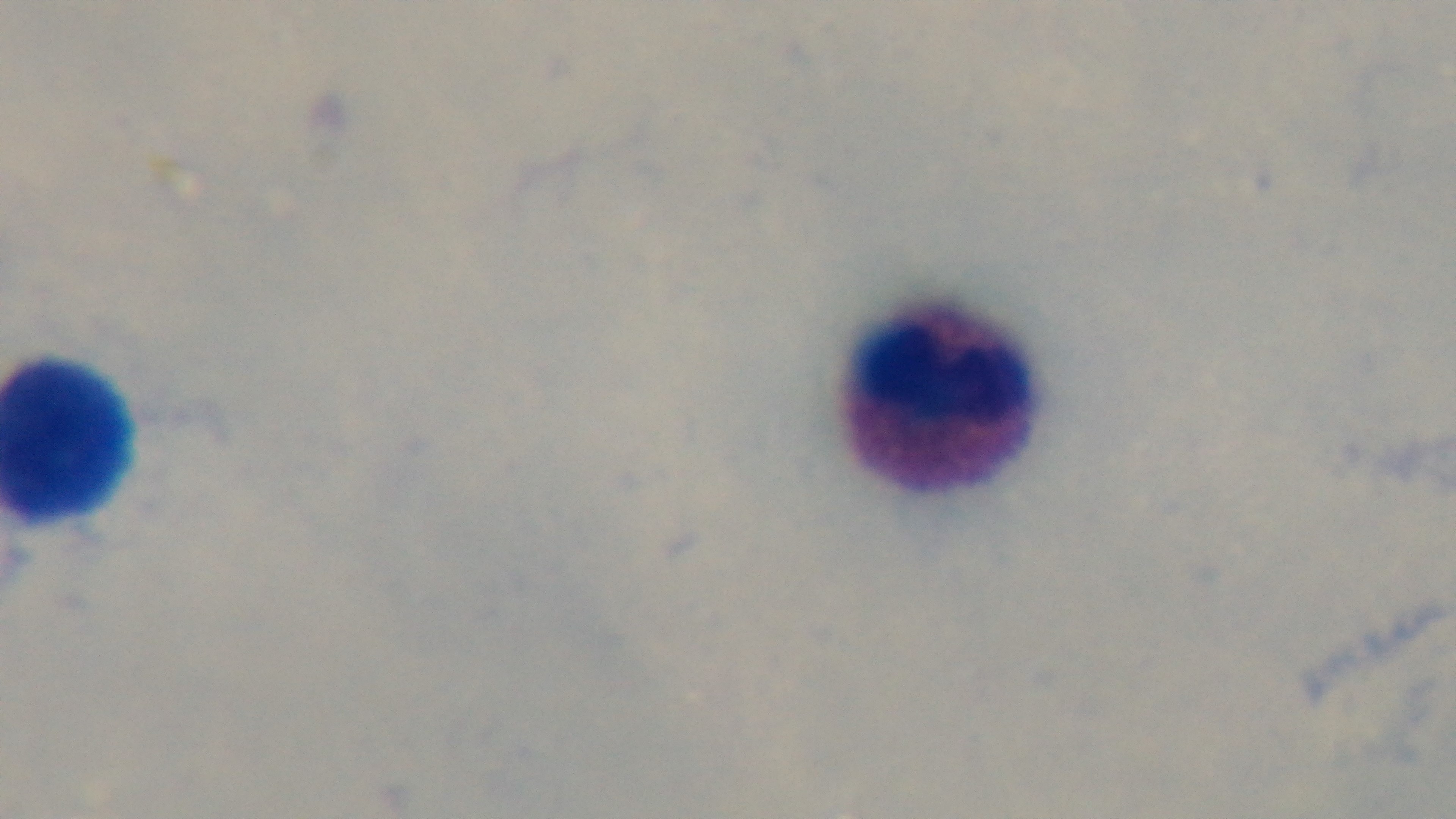

Summary:
  - Field of view: single
  - Objective: 100x oil immersion
  - Capture: mounted 4K digital camera
  - Modality: light microscopy
  - Stain: Giemsa
  - Preparation: thick
  - Malaria status: uninfected